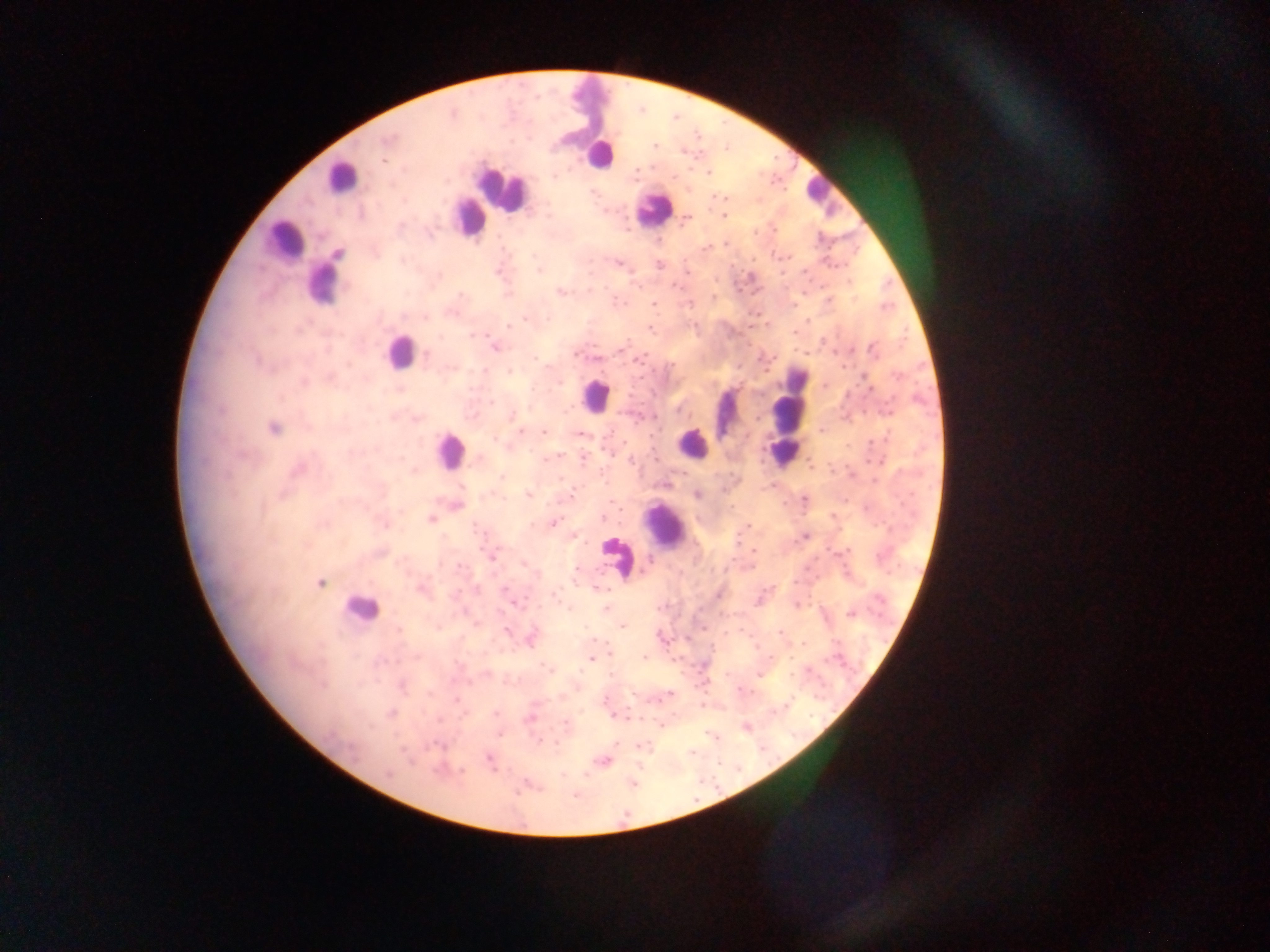 Approximate centers as [x, y] in pixels. Malaria parasite locations: [386, 140], [654, 145], [383, 161], [709, 173], [554, 177], [673, 177], [724, 216], [688, 218], [726, 244], [618, 263], [659, 265], [540, 271], [498, 272], [675, 286], [560, 292], [460, 295], [713, 297], [653, 303], [425, 318], [525, 318], [548, 318], [508, 327], [650, 328], [475, 334], [623, 348], [495, 349], [872, 349], [426, 354], [575, 354], [534, 358], [640, 358], [596, 359], [672, 365], [509, 372], [867, 381], [303, 382], [824, 386], [492, 403], [678, 411], [512, 414], [758, 418], [273, 428], [520, 431], [544, 432], [580, 435], [494, 439], [583, 458], [546, 459], [631, 461], [502, 477], [561, 478], [696, 494], [528, 495], [571, 497], [805, 499], [603, 518], [432, 519], [554, 523], [532, 524], [749, 524], [805, 536], [753, 550], [492, 557], [649, 560], [460, 565], [524, 565], [577, 570], [321, 583], [506, 588], [599, 589], [718, 594], [555, 597], [516, 605], [606, 609], [849, 614], [622, 627], [438, 628], [398, 629], [507, 631], [780, 633], [592, 640], [531, 641], [803, 643], [644, 657], [591, 659], [547, 668], [610, 674], [487, 675], [759, 675], [457, 699], [392, 713], [496, 714], [529, 719], [565, 723], [500, 735], [714, 738], [538, 740], [616, 744], [437, 745], [641, 745], [691, 752], [488, 760], [601, 760], [437, 769], [388, 775], [575, 795]. Leukocyte locations: [599, 155], [340, 177], [499, 190], [819, 191], [651, 209], [469, 217], [283, 240], [322, 285], [398, 351], [595, 395], [724, 415], [787, 421], [692, 444], [448, 452], [665, 525], [618, 556], [359, 609]. Sample from Ghana. Image is 1270×952 pixels. Mobile-phone photograph taken through the microscope. Thick blood film. Single field of view.